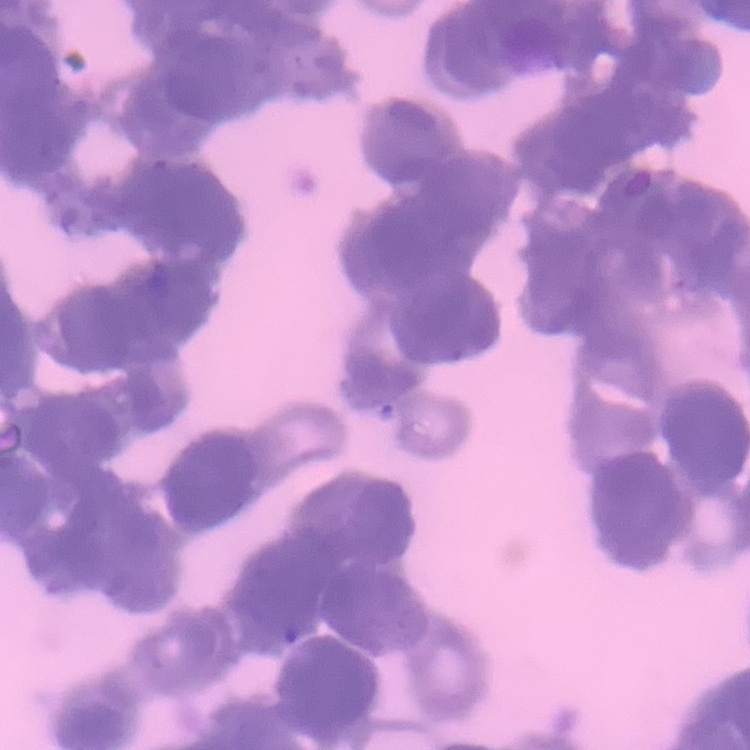
Summary:
  - Erythrocyte morphology: rouleaux formation
  - Image type: square crop of a larger photomicrograph
  - Stain: Field's or Giemsa
  - Preparation: thin peripheral smear